Assess this cell for malaria.
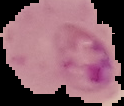

Parasitized.

Summary:
  - Image type: segmented cell region on a black background
  - Preparation: thin blood smear
  - Image size: 124×106 pixels